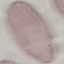

malaria status = uninfected
capture = smartphone through the microscope eyepiece
image type = cell patch, automatically extracted from a larger field of view and resized to 64 × 64 pixels
preparation = thin blood film
stain = Giemsa